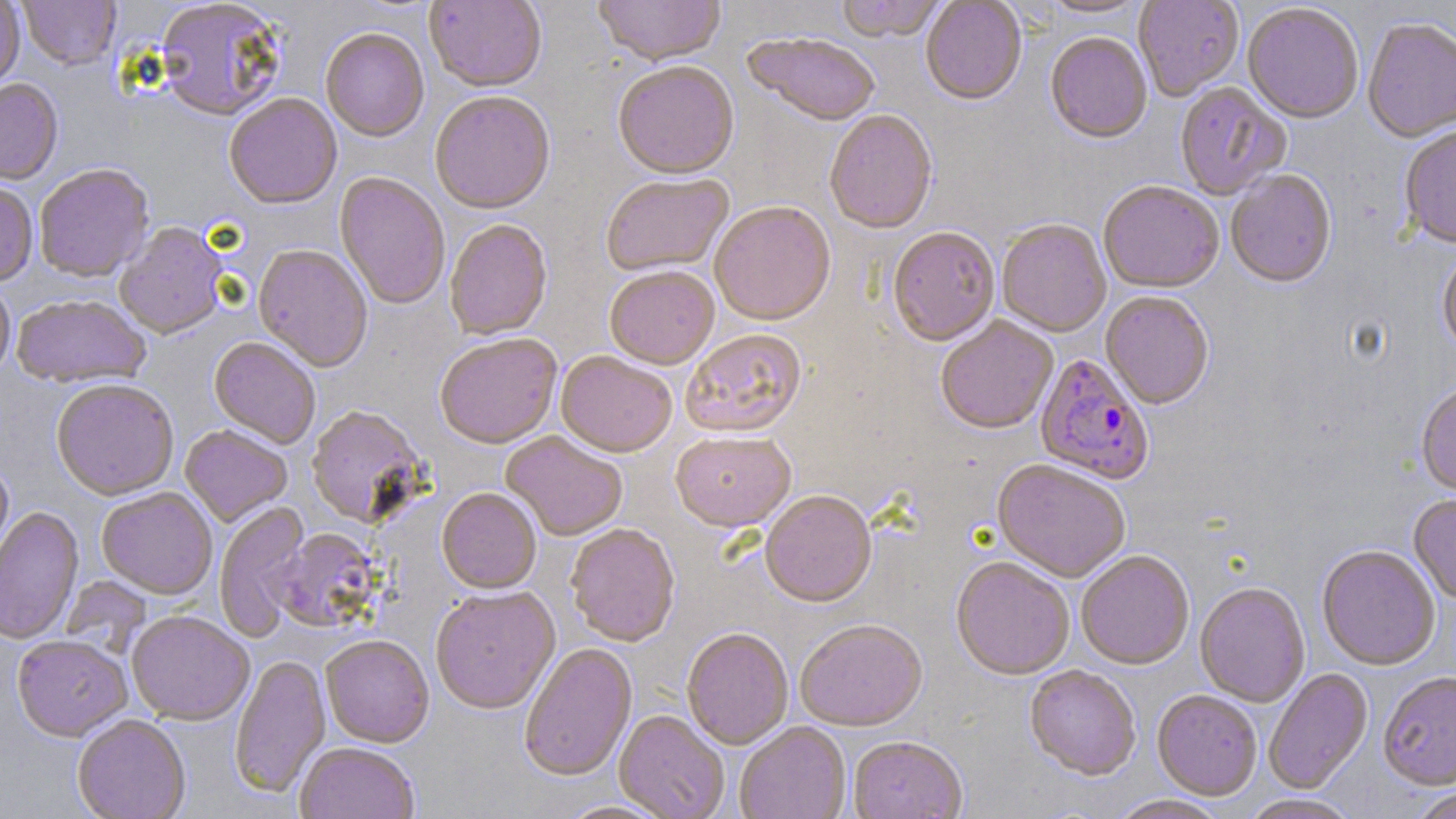

Approximate bounding boxes as [x1, y1, x2, y2] in pixels. Plasmodium falciparum-infected red blood cell locations: [1034, 354, 1154, 487]. Uninfected red blood cell locations: [19, 0, 120, 71], [424, 0, 547, 95], [593, 0, 725, 70], [836, 0, 948, 45], [1040, 0, 1150, 21], [1133, 0, 1244, 102], [0, 1, 25, 92], [154, 1, 286, 124], [920, 1, 1027, 108], [1243, 5, 1363, 126], [1362, 20, 1456, 144], [320, 30, 429, 144], [744, 35, 881, 129], [1045, 35, 1152, 146], [613, 63, 739, 183], [0, 80, 63, 187], [1175, 83, 1290, 201], [430, 93, 555, 217], [224, 95, 342, 212], [825, 111, 938, 237], [1399, 128, 1456, 250], [35, 165, 154, 284], [1226, 172, 1337, 291], [334, 173, 450, 311], [601, 175, 735, 278], [0, 183, 38, 288], [1099, 183, 1224, 295], [710, 203, 836, 328], [444, 221, 553, 342], [996, 221, 1111, 338], [115, 224, 229, 341], [887, 229, 1000, 349], [253, 245, 373, 374], [1437, 250, 1456, 358], [605, 269, 719, 372], [0, 280, 15, 385], [1100, 293, 1214, 411], [12, 296, 151, 389], [936, 318, 1058, 436], [681, 330, 807, 440], [435, 335, 562, 451], [208, 338, 320, 450], [556, 353, 676, 460], [51, 381, 179, 502], [1416, 385, 1456, 496], [306, 407, 429, 529], [180, 426, 292, 528], [501, 432, 627, 542], [670, 433, 796, 535], [0, 461, 14, 568], [991, 461, 1130, 584], [96, 488, 217, 600], [437, 489, 541, 596], [760, 493, 877, 610], [1408, 496, 1456, 605], [215, 502, 311, 642], [0, 508, 84, 645], [566, 525, 680, 649], [272, 528, 381, 634], [1317, 547, 1440, 672], [1076, 552, 1195, 671], [951, 559, 1075, 681], [60, 576, 151, 658], [1194, 584, 1310, 708], [431, 588, 560, 716], [126, 613, 254, 726], [795, 621, 928, 733], [682, 630, 794, 750], [12, 637, 133, 743], [321, 637, 434, 749], [518, 644, 638, 783], [230, 654, 331, 799], [1024, 667, 1141, 782], [1264, 668, 1373, 795], [1378, 673, 1456, 792], [1152, 691, 1262, 801], [613, 712, 729, 819], [73, 716, 191, 819], [735, 723, 850, 819], [848, 738, 967, 819], [295, 743, 419, 819], [1410, 786, 1456, 819], [1108, 795, 1231, 819], [1238, 795, 1361, 819], [554, 800, 677, 819]. Slide-level diagnosis: Plasmodium falciparum. 1000x magnification. May-Grünwald-Giemsa stain. Image is 1456×819 pixels. Single field of view. Light microscopy. Thin blood film.